Assess the morphology of the erythrocytes.
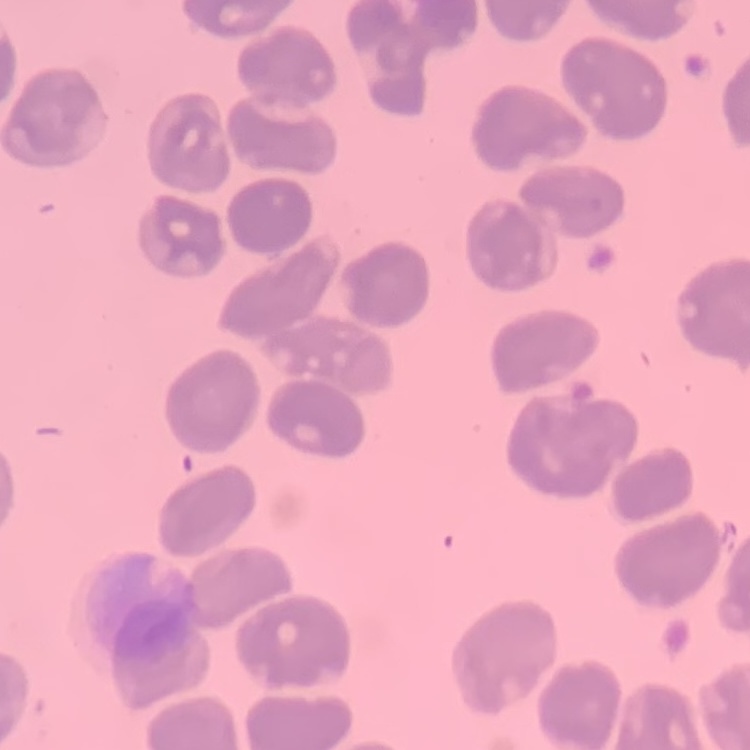

No rouleaux formation.

Summary:
  - Image type: one tile cut from a larger photomicrograph
  - Stain: Field's or Giemsa
  - Preparation: thin blood film